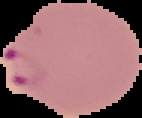
Summary:
  - Malaria status: parasitized
  - Image type: cell region segmented out of the field of view; surrounding area masked to black
  - Image size: 142×118 pixels
  - Preparation: thin blood smear